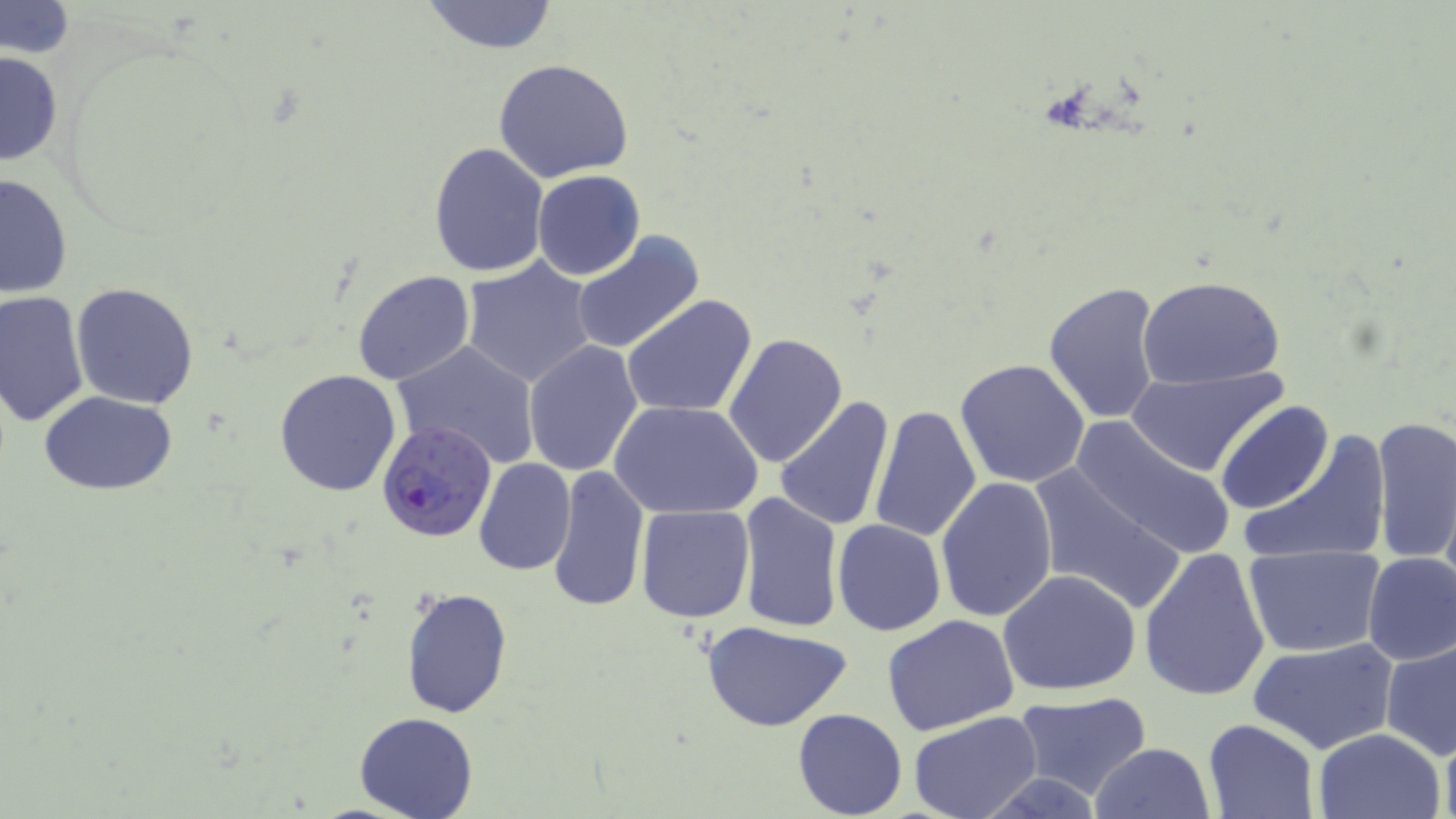
Summary:
  - Coordinate format: approximate bounding boxes as (x1,y1)-(x2,y2) corner pairs in pixels
  - Uninfected red blood cell locations: (418,0)-(562,54), (1,2)-(76,58), (0,48)-(62,169), (494,58)-(633,182), (428,142)-(549,278), (531,170)-(646,280), (0,172)-(73,301), (571,229)-(705,354), (460,258)-(599,389), (351,271)-(475,386), (1137,276)-(1288,387), (1045,281)-(1165,425), (71,282)-(199,408), (1,292)-(91,430), (623,295)-(757,419), (723,333)-(849,469), (390,339)-(542,469), (522,339)-(643,476), (955,358)-(1091,489), (1128,369)-(1286,477), (274,370)-(402,496), (38,390)-(178,495), (773,396)-(896,532), (610,401)-(763,520), (1214,401)-(1333,516), (868,403)-(981,544), (1072,416)-(1236,560), (1371,416)-(1455,565), (1239,429)-(1391,567), (472,458)-(578,576), (548,464)-(650,614), (1027,465)-(1187,619), (934,477)-(1056,622), (736,493)-(842,631), (635,505)-(755,623), (832,519)-(945,636), (1243,545)-(1388,658), (1138,546)-(1271,703), (1360,552)-(1456,666), (998,568)-(1142,697), (400,586)-(514,721), (882,615)-(1022,736), (702,621)-(851,733), (1247,636)-(1399,754), (1381,636)-(1456,761), (1013,692)-(1152,801), (793,708)-(907,818), (907,711)-(1043,819), (355,712)-(477,819), (1203,718)-(1320,819), (1312,727)-(1447,818), (1439,727)-(1456,819), (1087,742)-(1216,819)
  - Plasmodium falciparum-infected red blood cell locations: (375,418)-(499,544)
  - Slide-level diagnosis: Plasmodium falciparum
  - Field of view: single
  - Stain: May-Grünwald-Giemsa
  - Magnification: 1000x
  - Image size: 1456×819 pixels
  - Preparation: thin blood film
  - Modality: optical microscopy